Point out each Plasmodium parasite.
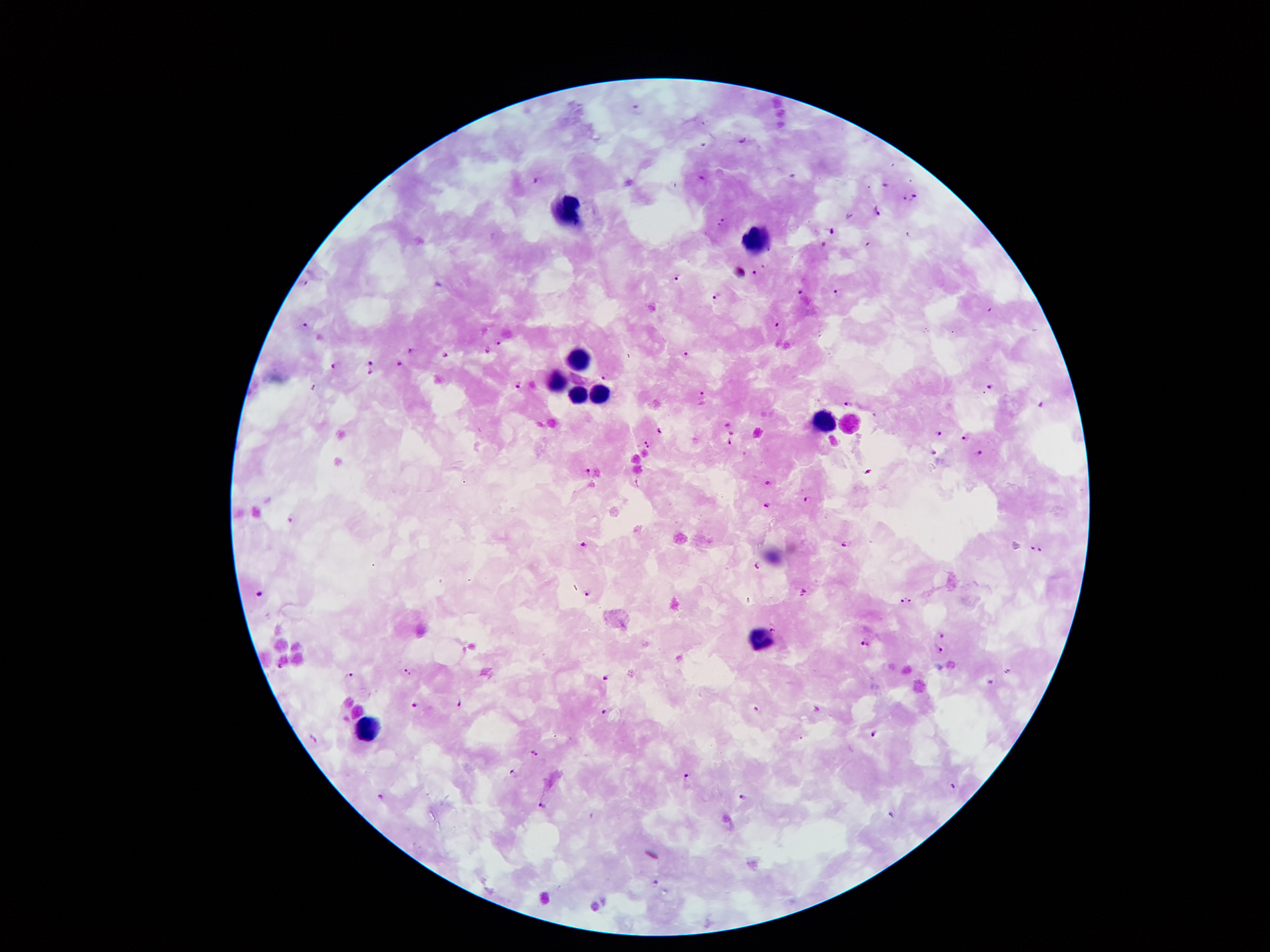

Approximate centers as (x, y) in pixels.
Plasmodium parasites: (742, 140), (538, 180), (885, 185), (905, 196), (913, 196), (877, 211), (723, 220), (831, 231), (753, 272), (678, 276), (305, 282), (799, 291), (836, 291), (715, 296), (777, 322), (305, 323), (498, 341), (411, 348), (488, 350), (687, 353), (445, 354), (372, 362), (400, 362), (335, 365), (371, 372), (604, 376), (520, 385), (988, 387), (704, 392), (848, 403), (1042, 406), (660, 430), (733, 433), (939, 433), (964, 438), (647, 441), (731, 443), (979, 451), (934, 454), (588, 470), (868, 472), (769, 482), (807, 499), (765, 505), (291, 518), (848, 543), (585, 545), (1033, 547), (1041, 550), (758, 566), (261, 592), (587, 593), (803, 593), (911, 599), (902, 601), (772, 629), (940, 635), (863, 645), (940, 649), (406, 670), (1009, 671), (350, 674), (605, 678), (992, 682), (460, 703), (417, 704), (758, 709), (605, 711), (874, 732), (312, 738), (533, 754), (512, 773), (687, 775), (954, 785), (382, 796), (742, 797), (542, 804), (893, 815), (655, 883).

{
  "preparation": "thick peripheral-blood smear",
  "field_of_view": "one from this slide",
  "magnification": "100x",
  "leukocyte_locations": "approximate centers as (x, y) in pixels: (565, 208), (757, 241), (580, 356), (558, 379), (599, 391), (576, 392), (824, 417), (853, 423), (760, 636), (364, 729)",
  "capture": "smartphone through the microscope eyepiece",
  "stain": "Giemsa",
  "patient_malaria_status": "infected with Plasmodium falciparum",
  "image_size": "1270×952 pixels"
}